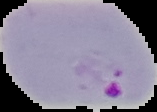
{
  "image_size": "157×112 pixels",
  "image_type": "segmented cell region with the area outside set to black",
  "preparation": "thin blood smear",
  "malaria_status": "parasitized"
}